Give a bounding box for every parasitised red blood cell, every trophozoite, every gametocyte, every leukocyte, and every artifact (platelet-like body, stain precipitate, or debris).
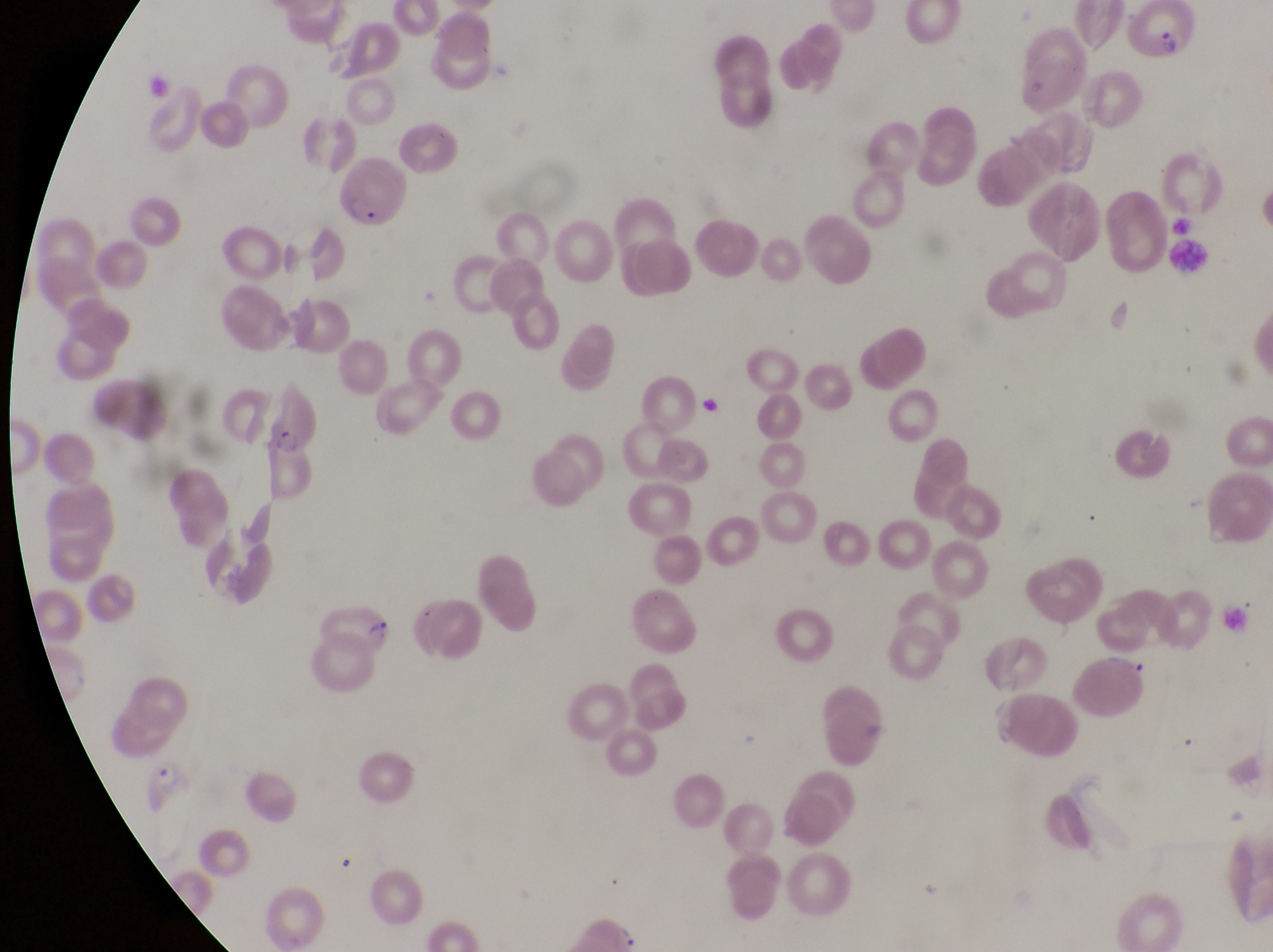
Approximate bounding boxes as {left, top, right, bottom} in pixels.
Parasitised red blood cells: {1131, 2, 1205, 72}, {340, 157, 412, 237}, {262, 394, 322, 462}, {310, 596, 395, 663}, {147, 759, 199, 817}.
No leukocytes observed.

Summary:
  - Country: Uganda
  - Capture: smartphone photograph through the eyepiece of an Olympus CX-23 microscope
  - Image size: 1273×952 pixels
  - Magnification: 1000x
  - Preparation: thin blood film
  - Field of view: single